Look for Plasmodium parasites.
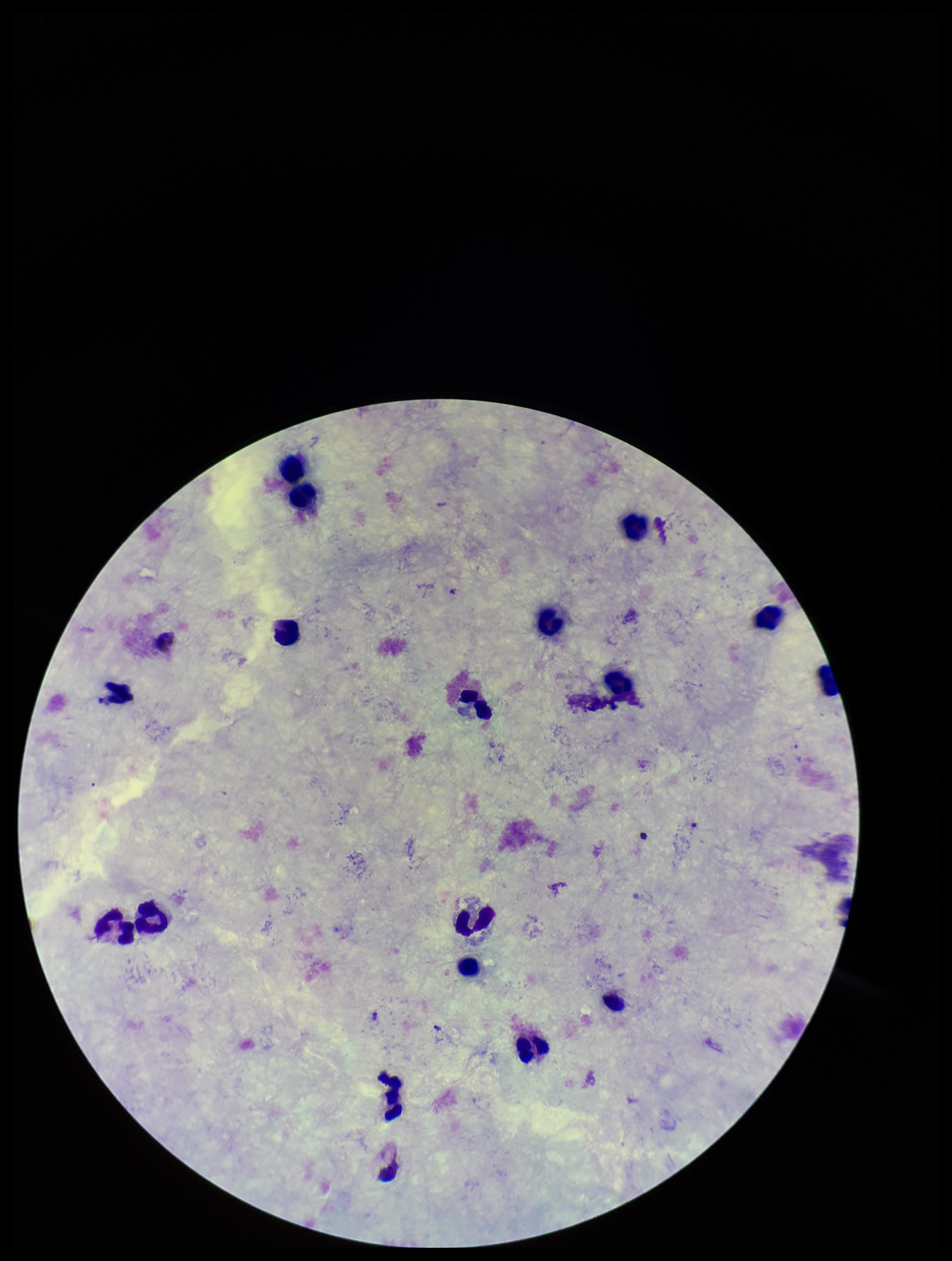
None seen.

leukocyte_count: 18
capture: smartphone photograph through the microscope eyepiece
field_of_view: one from this slide
stain: Giemsa
species_reported_for_this_patient: Plasmodium vivax
patient_malaria_status: infected
image_size: 952×1261 pixels
preparation: thick smear
parasite_count: 0